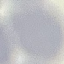

Summary:
  - Malaria status: uninfected
  - Stain: Giemsa
  - Preparation: thin blood smear
  - Capture: smartphone through the microscope eyepiece
  - Image type: cell patch, automatically extracted from a larger field of view and resized to 64 × 64 pixels